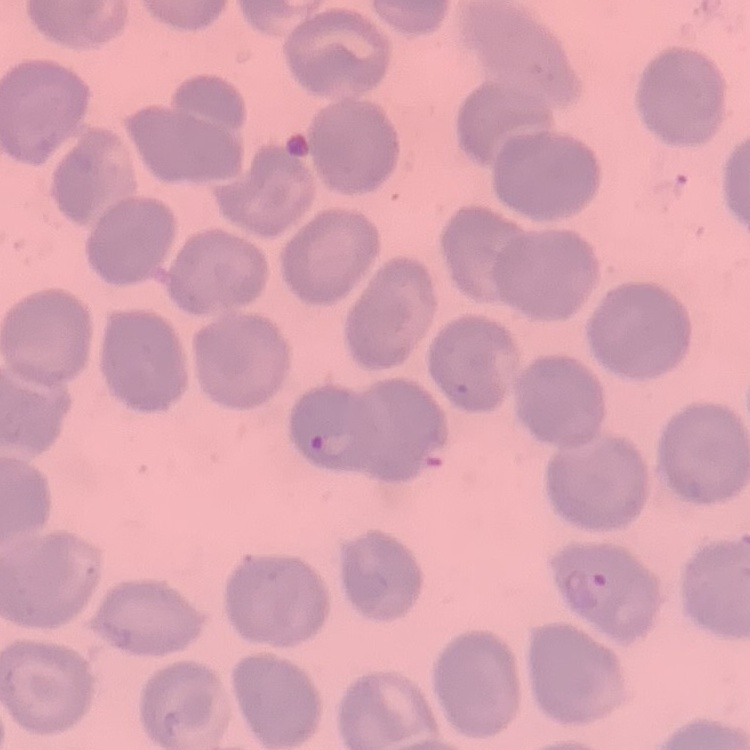 The erythrocytes exhibit no rouleaux formation. Thin peripheral smear. Field's or Giemsa stain. One tile cut from a larger photomicrograph.